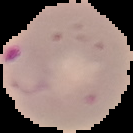
preparation: thin blood film
image_type: segmented cell region on a black background
malaria_status: parasitized
image_size: 133×133 pixels